Locate every uninfected red blood cell.
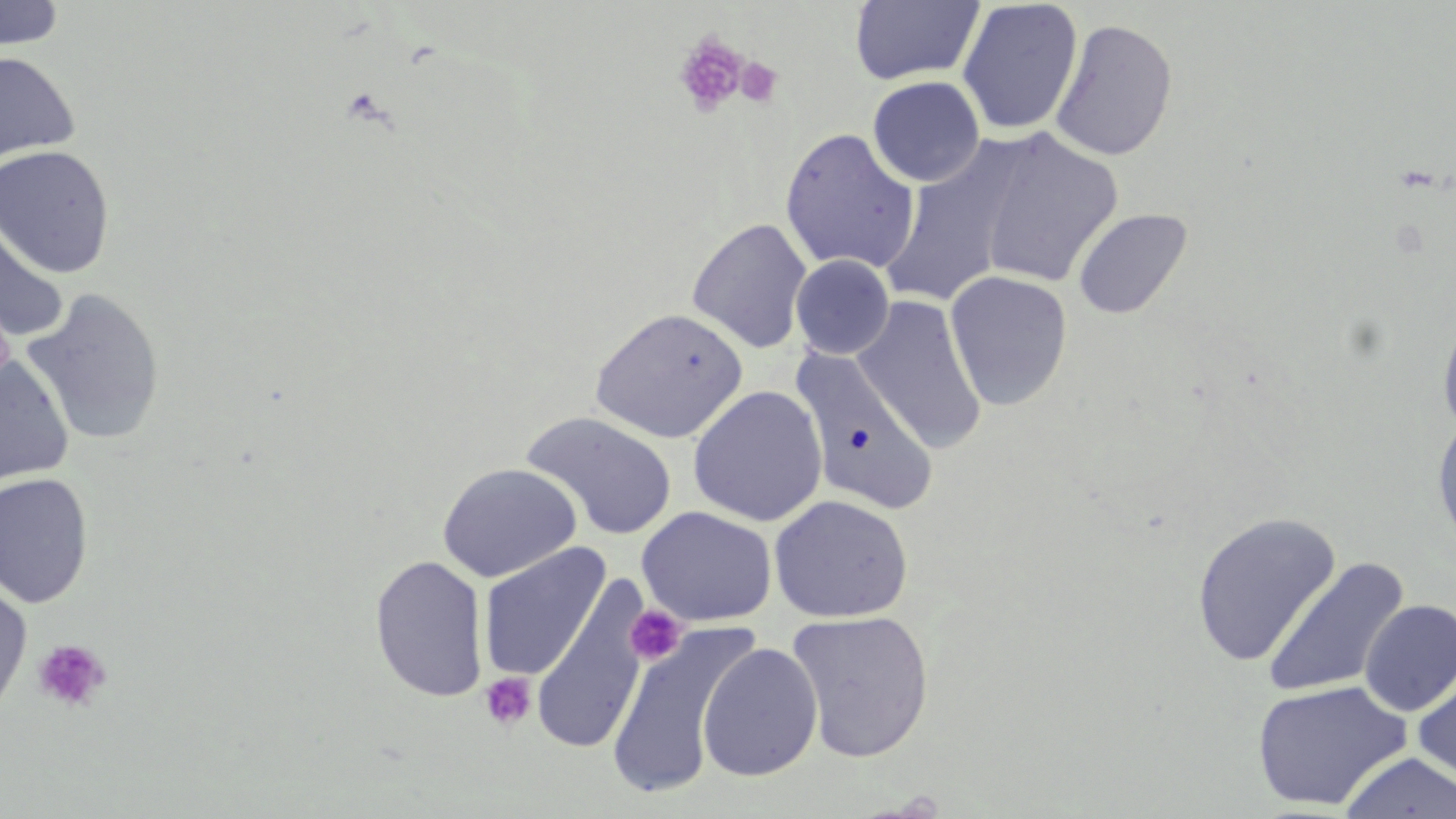

Approximate bounding boxes as named x1/y1/x2/y2 corners in pixels.
Uninfected red blood cells: (x1=0, y1=1, x2=67, y2=51), (x1=850, y1=1, x2=985, y2=86), (x1=957, y1=1, x2=1084, y2=136), (x1=1050, y1=18, x2=1178, y2=162), (x1=0, y1=50, x2=81, y2=163), (x1=867, y1=76, x2=985, y2=187), (x1=779, y1=127, x2=921, y2=274), (x1=975, y1=129, x2=1124, y2=290), (x1=880, y1=143, x2=1028, y2=308), (x1=0, y1=144, x2=116, y2=278), (x1=1073, y1=208, x2=1193, y2=320), (x1=0, y1=216, x2=70, y2=344), (x1=687, y1=218, x2=812, y2=353), (x1=790, y1=254, x2=894, y2=359), (x1=944, y1=269, x2=1073, y2=411), (x1=21, y1=286, x2=166, y2=448), (x1=852, y1=296, x2=987, y2=454), (x1=1436, y1=305, x2=1456, y2=442), (x1=589, y1=308, x2=748, y2=443), (x1=791, y1=349, x2=939, y2=516), (x1=0, y1=356, x2=75, y2=484), (x1=688, y1=385, x2=828, y2=527), (x1=520, y1=411, x2=677, y2=541), (x1=1431, y1=415, x2=1456, y2=554), (x1=437, y1=462, x2=582, y2=582), (x1=0, y1=472, x2=94, y2=608), (x1=769, y1=494, x2=914, y2=623), (x1=636, y1=506, x2=777, y2=626), (x1=1191, y1=511, x2=1341, y2=667), (x1=477, y1=542, x2=611, y2=682), (x1=369, y1=555, x2=490, y2=703), (x1=1262, y1=557, x2=1410, y2=699), (x1=530, y1=577, x2=650, y2=757), (x1=0, y1=580, x2=33, y2=721), (x1=1359, y1=599, x2=1456, y2=716), (x1=786, y1=610, x2=935, y2=763), (x1=606, y1=621, x2=756, y2=801), (x1=697, y1=642, x2=823, y2=781), (x1=1412, y1=659, x2=1456, y2=790), (x1=1250, y1=679, x2=1412, y2=811), (x1=1339, y1=752, x2=1456, y2=818).

{
  "slide_level_diagnosis": "no evidence of blood parasites",
  "preparation": "thin blood smear",
  "stain": "May-Grünwald-Giemsa",
  "modality": "light microscopy",
  "platelet_locations": "approximate bounding boxes as named x1/y1/x2/y2 corners in pixels: (x1=674, y1=30, x2=748, y2=118), (x1=735, y1=57, x2=782, y2=108), (x1=624, y1=604, x2=687, y2=666), (x1=33, y1=637, x2=112, y2=713), (x1=479, y1=672, x2=537, y2=732)",
  "image_size": "1456×819 pixels",
  "field_of_view": "one of a larger specimen",
  "magnification": "1000x"
}